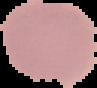 The area outside the segmented cell region is set to black. Image is 97×88 pixels. Malaria status: uninfected. From a thin blood smear.